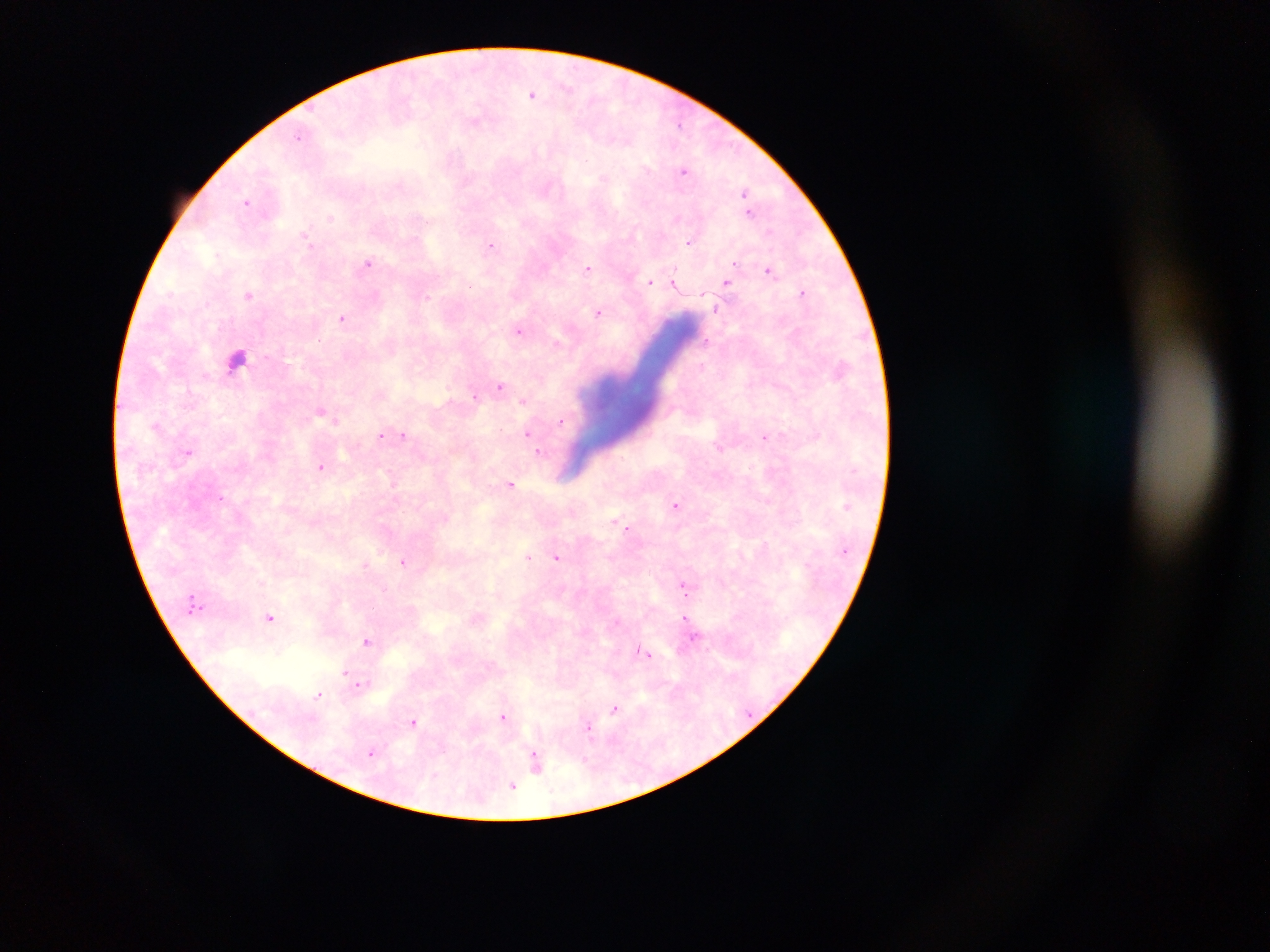

preparation = thick blood film
capture = mobile-phone photograph through a microscope
country = Ghana
Plasmodium parasite locations = approximate centers as x y in pixels: 533 94; 680 123; 299 137; 684 170; 745 193; 248 201; 748 202; 750 211; 330 217; 677 218; 689 241; 491 244; 369 262; 590 268; 769 270; 650 281; 674 282; 727 282; 803 292; 250 294; 717 308; 600 312; 342 318; 520 329; 707 340; 558 344; 237 358; 501 385; 475 394; 524 400; 322 410; 561 421; 528 432; 403 434; 381 435; 392 435; 766 435; 189 451; 538 451; 321 466; 512 484; 677 505; 629 528; 529 557; 557 557; 403 560; 366 564; 685 586; 271 618; 687 618; 367 640; 643 651; 345 672; 359 684; 320 694; 615 709; 504 717; 414 721; 590 729; 371 752; 537 760; 512 785
image size = 1270×952 pixels
field of view = single